Describe the morphology of the erythrocytes.
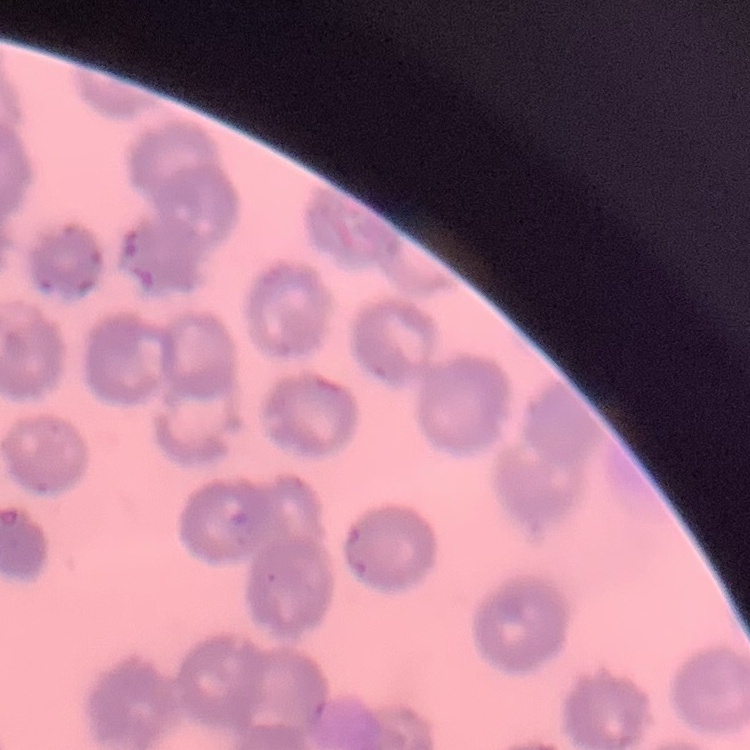
No rouleaux formation.

Summary:
  - Preparation: thin blood smear
  - Image type: one tile cut from a larger photomicrograph
  - Stain: Field's or Giemsa